Name the parasite shown.
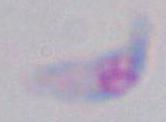
Toxoplasma gondii.

Summary:
  - Modality: photomicrograph
  - Magnification: 1000x